Assess for Plasmodium parasites.
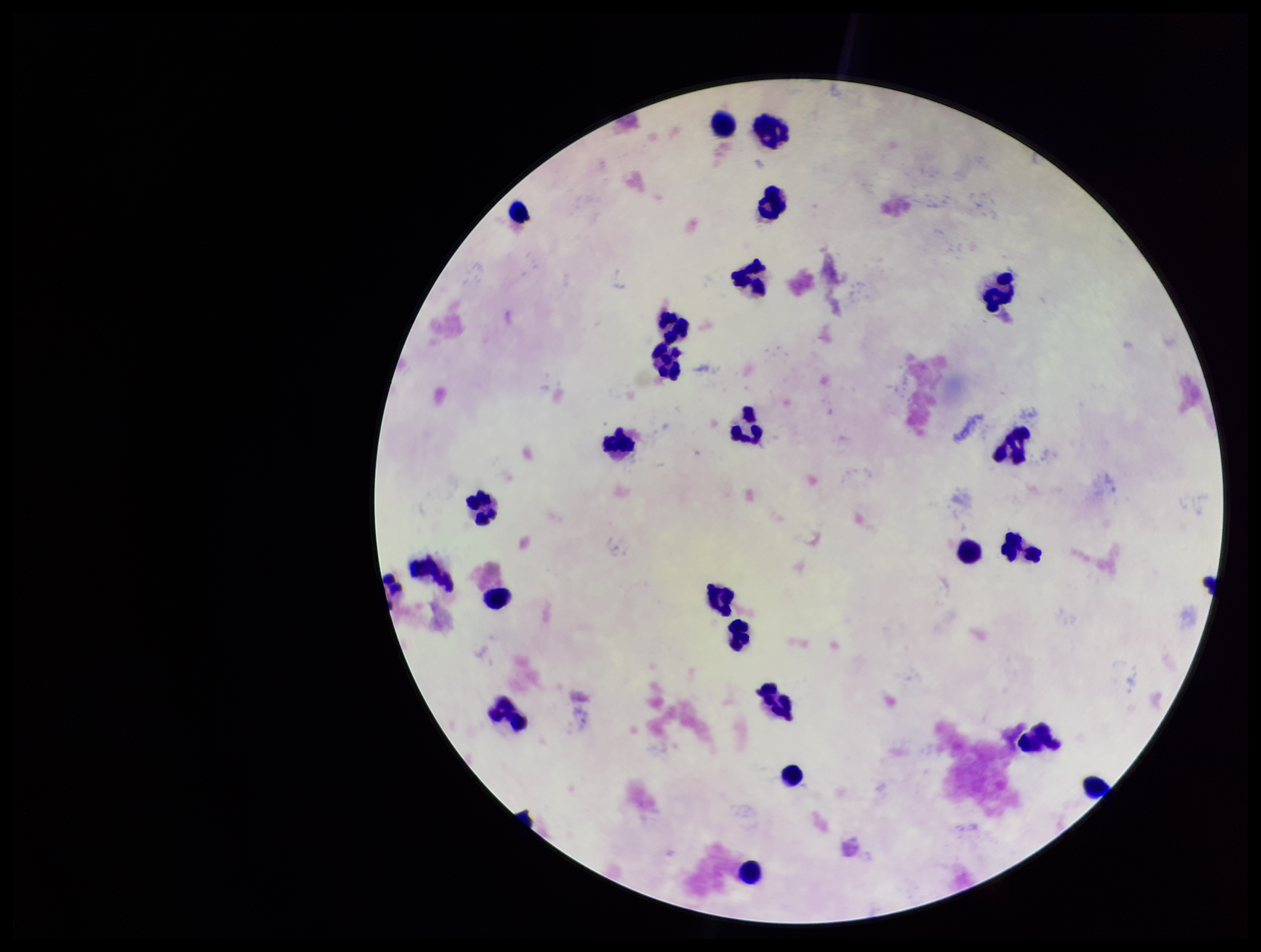

None identified.

Parasite count: 0. Preparation: thick blood smear. Image is 1261×952 pixels. Stained with Giemsa. Patient malaria status: negative. Photographed through the microscope eyepiece with a smartphone camera. Single field of view. Leukocyte count: 23.